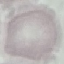
Summary:
  - Result: no malaria parasites detected
  - Preparation: thin blood film
  - Capture: smartphone camera at the microscope eyepiece
  - Stain: Giemsa
  - Image type: automatically extracted cell patch, resized to 64 × 64 pixels